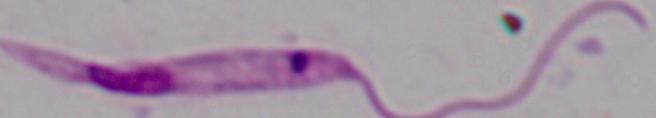

Summary:
  - Identification: Leishmania
  - Magnification: 1000x
  - Modality: photomicrograph